State the preparation type.
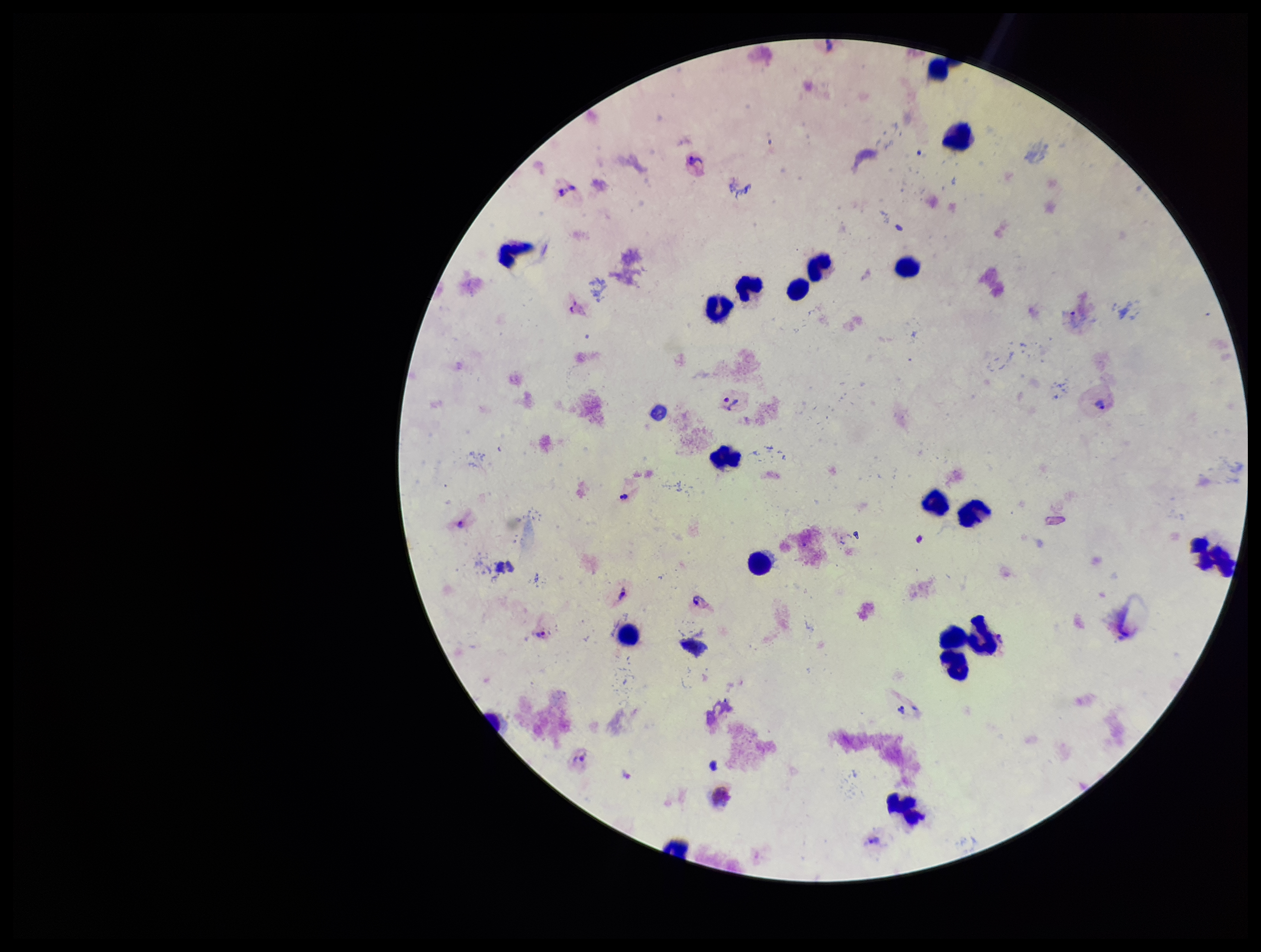
Thick.

Summary:
  - Leukocyte count: 18
  - Parasite count: 8
  - Patient malaria status: infected
  - Field of view: one from this slide
  - Capture: smartphone photograph through the microscope eyepiece
  - Species reported for this patient: Plasmodium vivax
  - Image size: 1261×952 pixels
  - Plasmodium parasites: identified
  - Stain: Giemsa